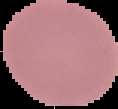
Summary:
  - Image size: 118×109 pixels
  - Result: no Plasmodium parasites detected
  - Preparation: thin blood film
  - Image type: segmented cell region on a black background